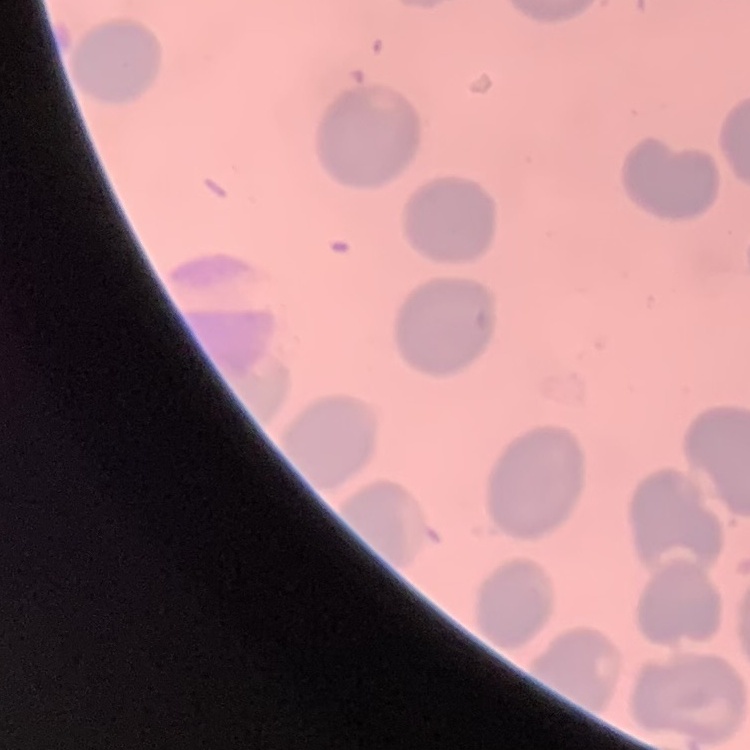
The erythrocytes exhibit no rouleaux formation. Stained with either Field's or Giemsa. Square crop of a larger photomicrograph. Thin blood smear.